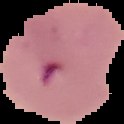

preparation = thin blood smear
malaria status = parasitized
image type = cell region segmented out of the field of view; surrounding area masked to black
image size = 124×124 pixels